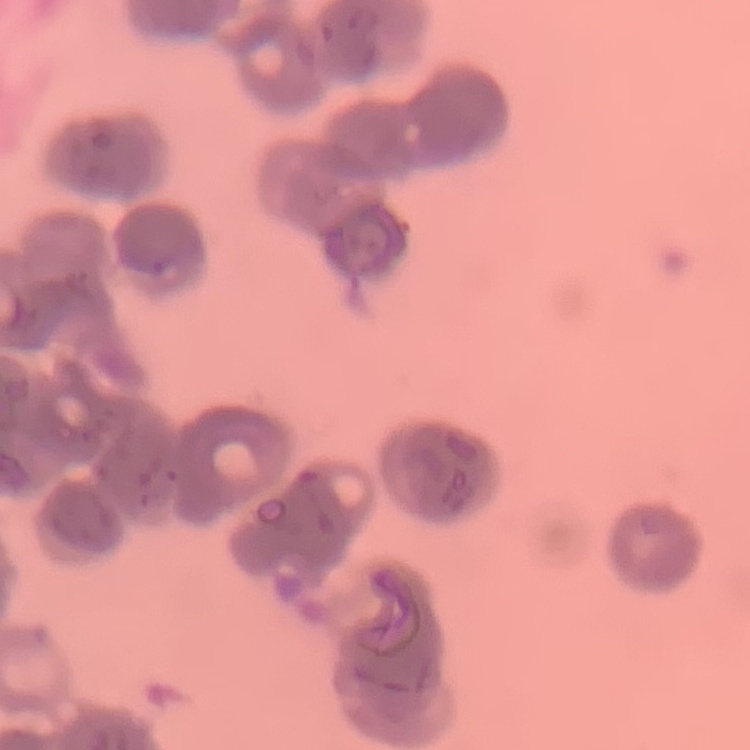 The erythrocytes exhibit rouleaux formation. One tile cut from a larger photomicrograph. Stained with either Field's or Giemsa. Thin peripheral smear.